Mark where leukocytes are.
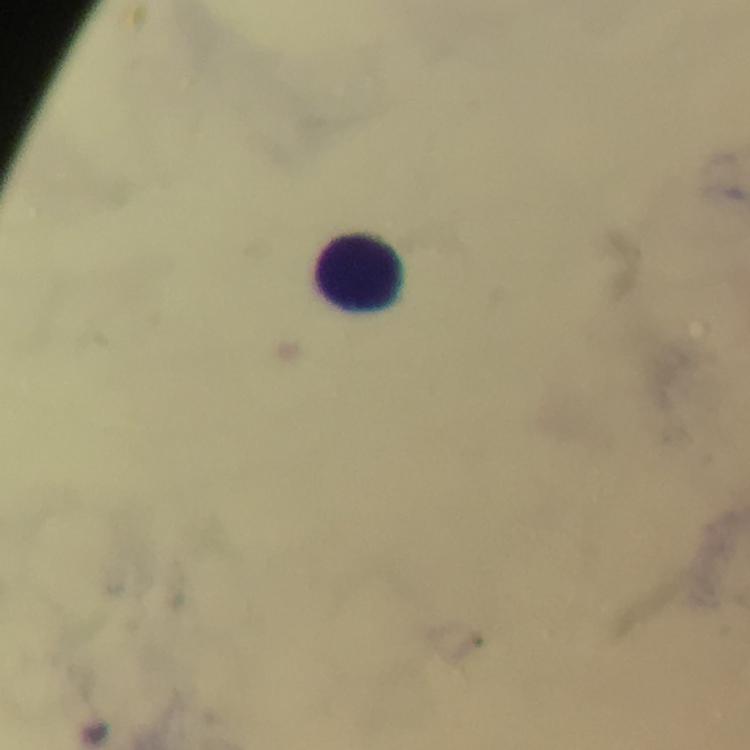

Approximate centers as {x, y} in pixels.
Leukocytes: {360, 273}.

Giemsa-stained preparation. Malaria parasites: none seen. Cropped region of a single field of view. Image is 750×750 pixels. 100x magnification. From a diagnostic examination for malaria. Thick smear. Immersion oil applied. Photographed with a smartphone mounted on the microscope.